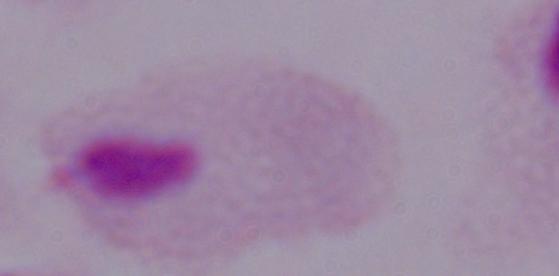
identification = trichomonad
magnification = 1000x
modality = photomicrograph